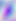
identification = Toxoplasma gondii
modality = micrograph
magnification = 400x